Report the malaria status.
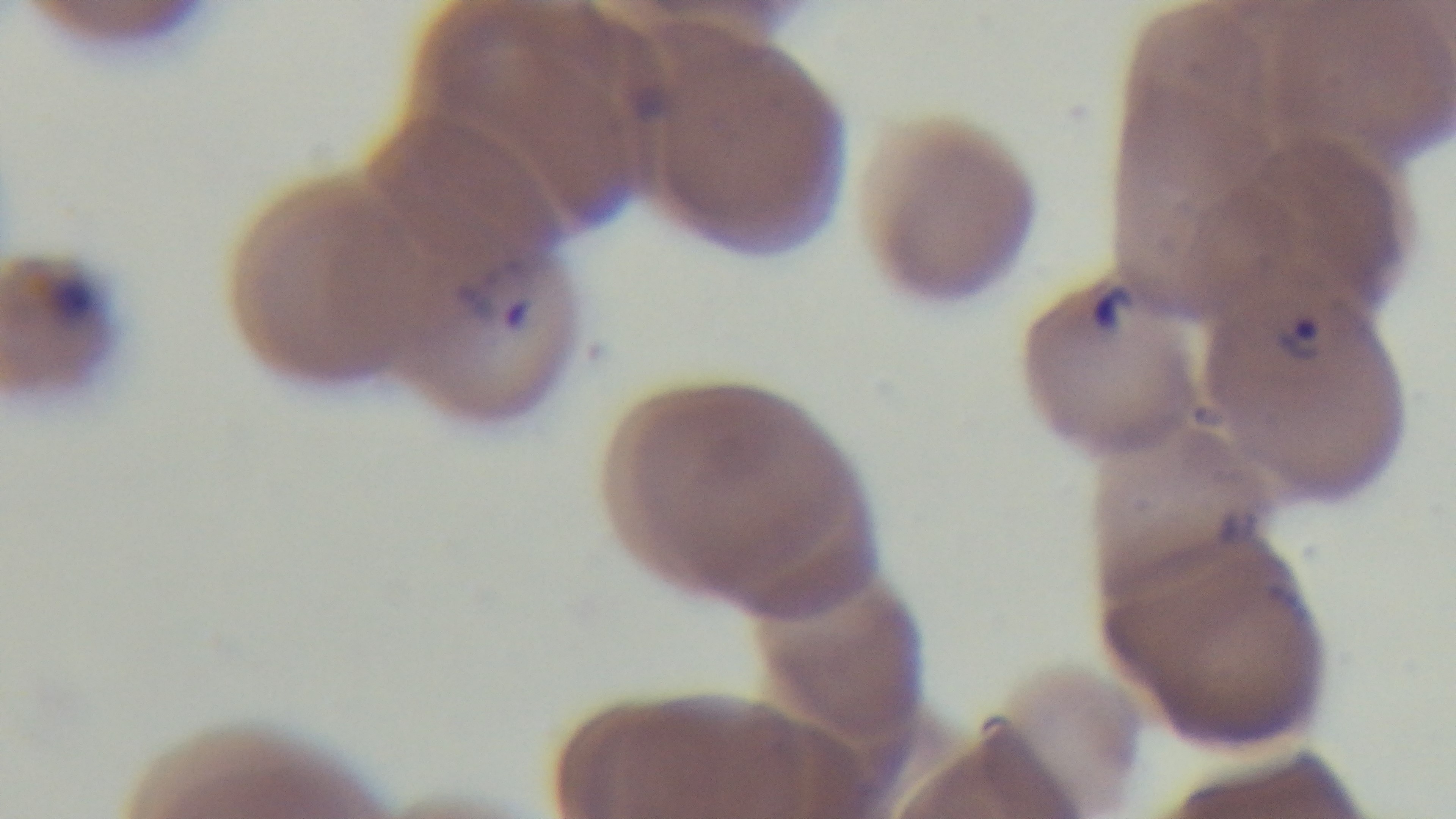

Positive.

stain = Giemsa
modality = light microscopy
objective = 100x oil immersion
field of view = one from the slide
capture = mounted 4K digital camera
preparation = thin smear